Mark where leukocytes are.
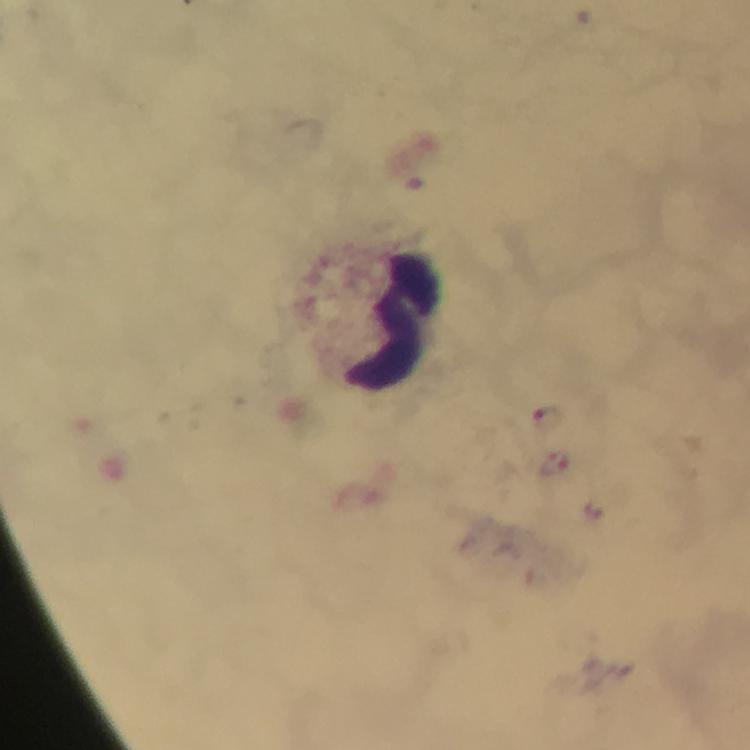

Approximate centers as (x, y) in pixels.
Leukocytes: (392, 322).

Plasmodium parasite locations: (549, 418), (552, 468). From a diagnostic examination for malaria. Immersion oil applied. At 100x magnification. Thick smear. Cropped region of a single field of view. Image is 750×750 pixels. Photographed through the microscope with a smartphone camera. Giemsa-stained preparation.